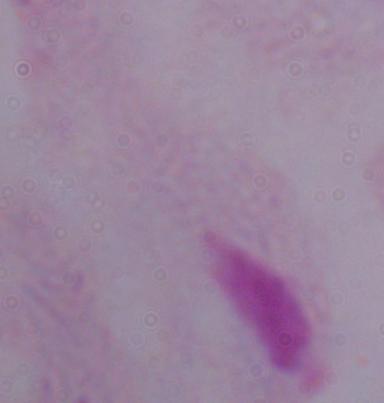

Captured at 1000x magnification. Micrograph. A trichomonad is shown.